Locate every leukocyte (white blood cell).
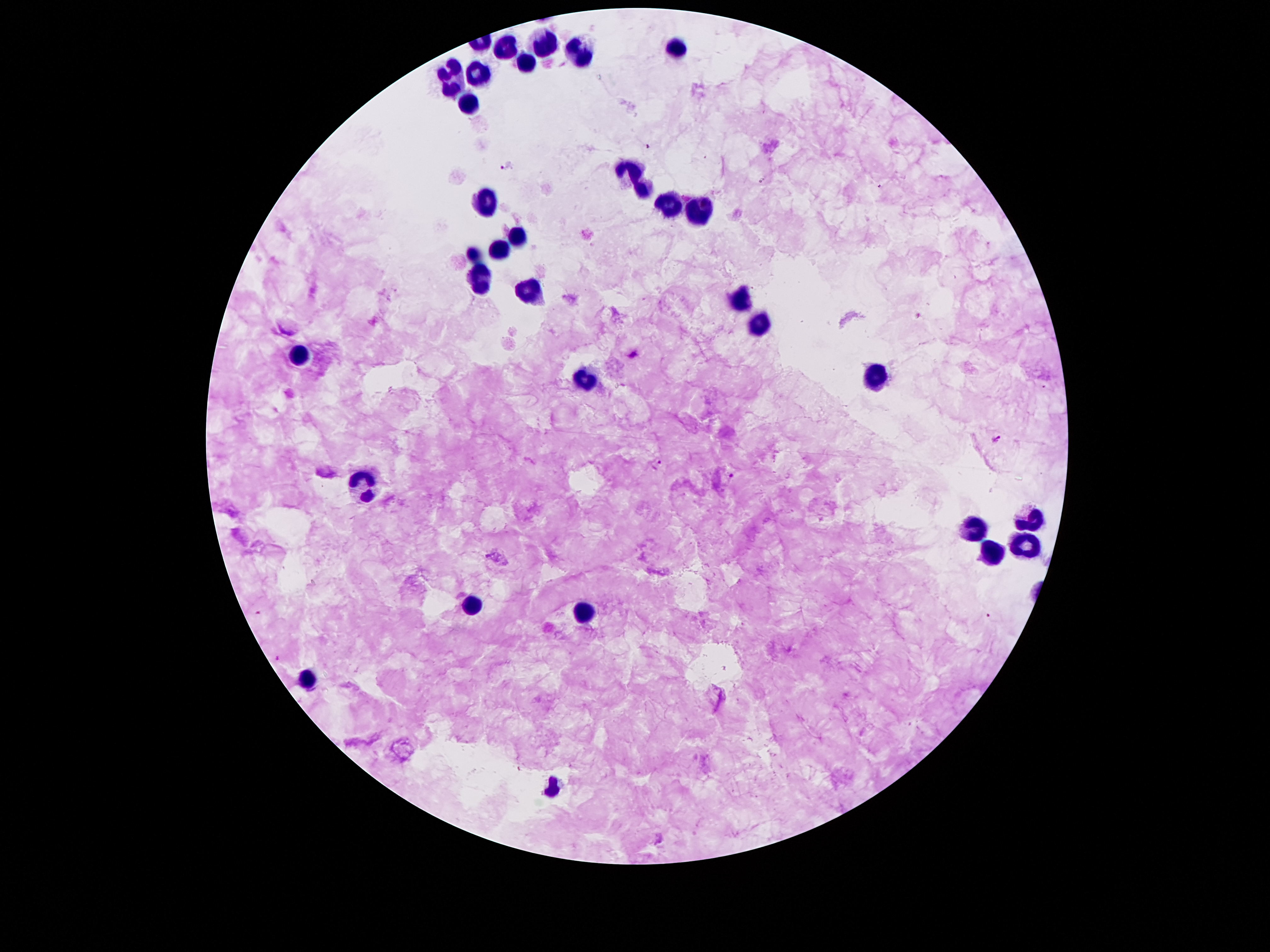

Approximate centers as {x, y} in pixels.
Leukocytes: {543, 43}, {678, 46}, {506, 49}, {580, 53}, {524, 60}, {453, 70}, {479, 74}, {469, 97}, {633, 170}, {643, 191}, {483, 201}, {670, 205}, {700, 209}, {516, 236}, {498, 247}, {471, 254}, {481, 279}, {530, 291}, {737, 301}, {762, 324}, {299, 352}, {874, 377}, {584, 381}, {363, 477}, {1032, 514}, {975, 529}, {1028, 540}, {993, 557}, {471, 605}, {580, 611}, {307, 679}, {553, 788}.

Summary:
  - Plasmodium parasite locations: {646, 148}, {507, 167}, {919, 316}, {997, 439}, {659, 464}, {734, 476}, {259, 613}, {989, 615}, {276, 659}
  - Capture: smartphone through the microscope eyepiece
  - Magnification: 100x
  - Stain: Giemsa
  - Patient malaria status: infected with Plasmodium falciparum
  - Image size: 1270×952 pixels
  - Preparation: thick blood film
  - Field of view: single